Assess this cell for malaria.
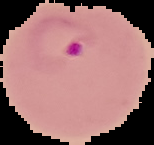

It is parasitized.

image size = 154×145 pixels
image type = segmented cell region with the area outside set to black
preparation = thin blood smear